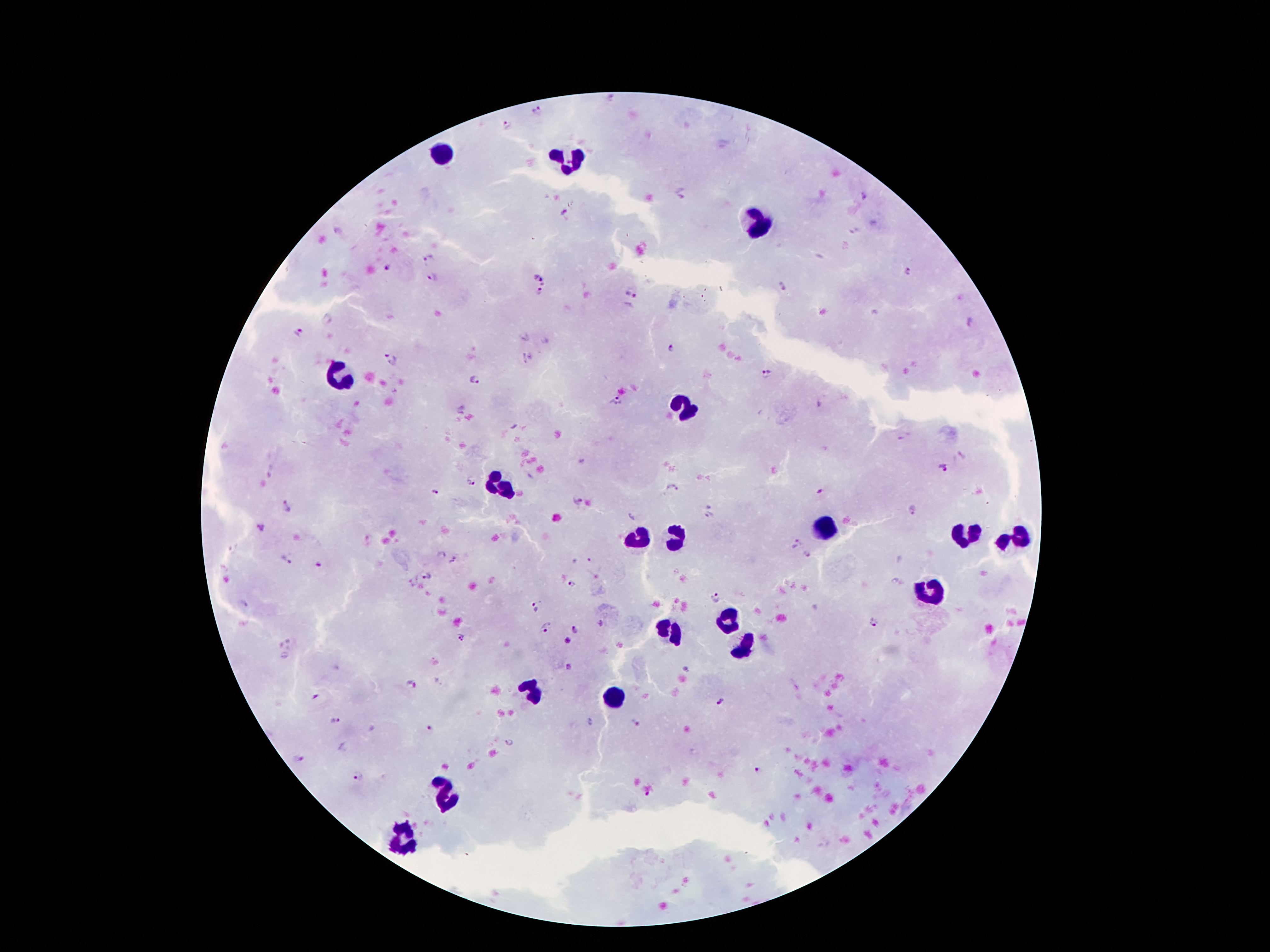
Approximate centers as {x, y} in pixels. Plasmodium parasite locations: {538, 110}, {507, 126}, {682, 194}, {864, 194}, {563, 215}, {430, 257}, {389, 267}, {908, 273}, {433, 276}, {538, 277}, {783, 287}, {629, 291}, {541, 292}, {327, 319}, {300, 330}, {673, 348}, {391, 360}, {768, 373}, {473, 380}, {616, 400}, {942, 466}, {473, 481}, {673, 486}, {818, 489}, {433, 492}, {576, 502}, {286, 506}, {912, 509}, {711, 513}, {261, 527}, {796, 543}, {807, 554}, {285, 558}, {321, 564}, {428, 575}, {572, 584}, {714, 600}, {241, 604}, {533, 610}, {874, 623}, {545, 628}, {575, 631}, {461, 637}, {566, 641}, {570, 668}, {688, 669}, {410, 685}, {317, 697}, {721, 704}, {337, 721}, {636, 726}, {430, 729}, {510, 742}, {299, 760}, {760, 769}, {359, 775}, {648, 793}. Leukocyte locations: {442, 154}, {567, 160}, {752, 223}, {339, 372}, {684, 410}, {500, 487}, {827, 529}, {640, 537}, {967, 538}, {676, 540}, {1018, 540}, {931, 591}, {730, 621}, {671, 629}, {746, 646}, {533, 693}, {615, 696}, {448, 793}, {405, 839}. 100x magnification. One field from this slide. Giemsa stain. Image is 1270×952 pixels. Thick blood film. Patient malaria status: positive for Plasmodium falciparum. Photographed through the microscope eyepiece with a smartphone camera.